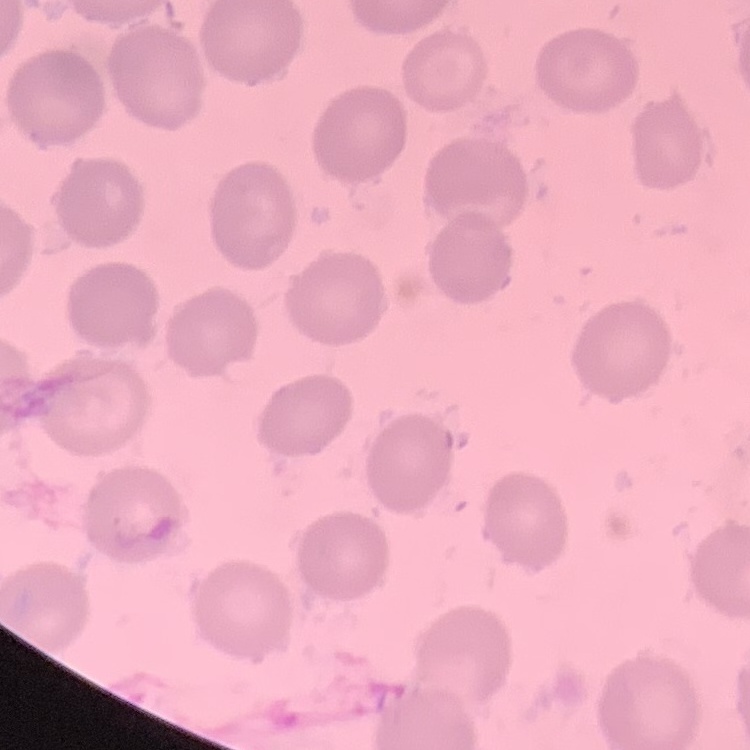
Summary:
  - Erythrocyte morphology: no rouleaux formation
  - Stain: Field's or Giemsa
  - Preparation: thin peripheral smear
  - Image type: square crop of a larger photomicrograph